Name the parasite shown.
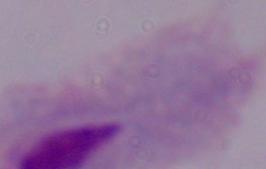
This is a trichomonad.

Summary:
  - Modality: micrograph
  - Magnification: 1000x